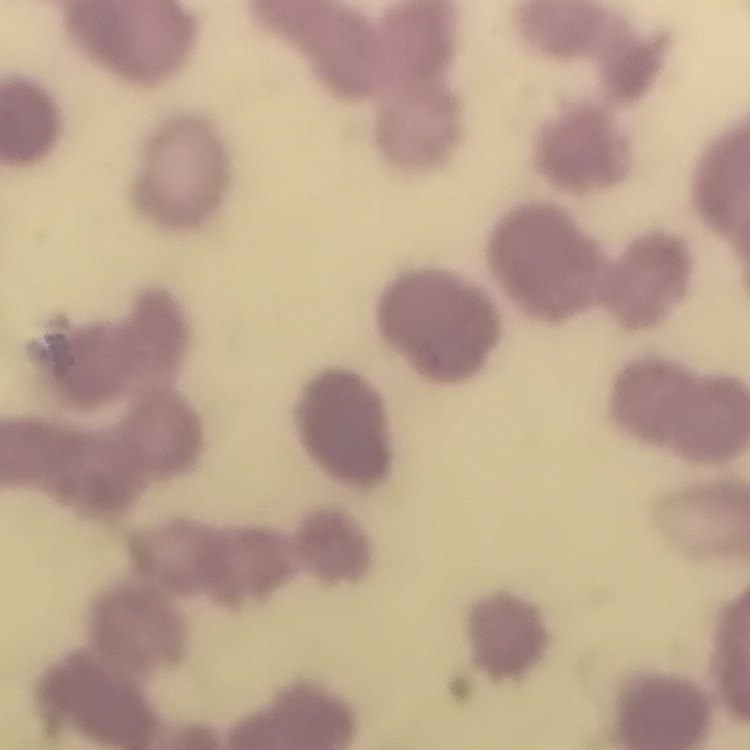

The erythrocytes exhibit rouleaux formation. Stained with either Field's or Giemsa. Thin blood film. One tile cut from a larger photomicrograph.